State the preparation type.
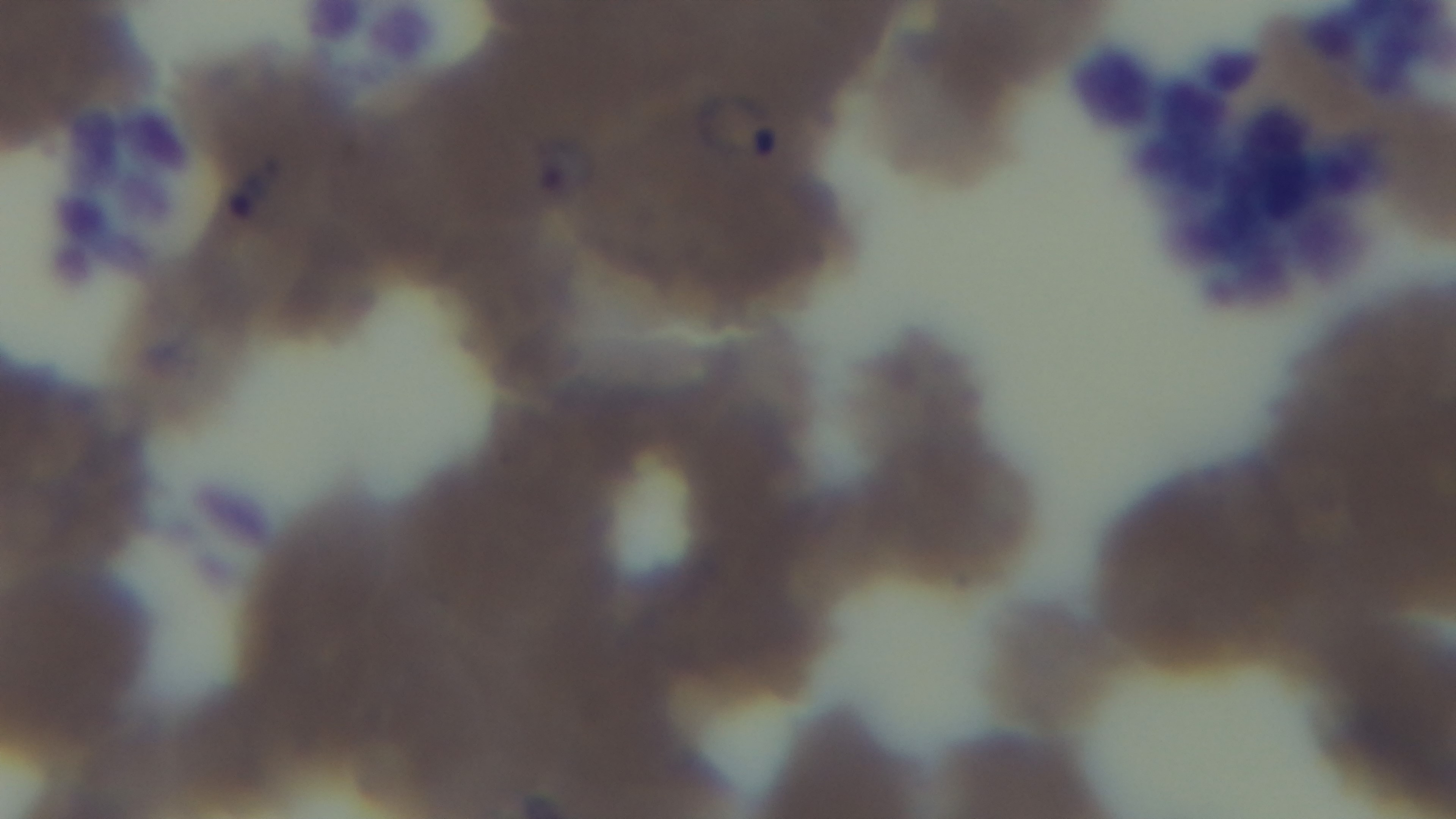

A thin smear.

One field from the slide. Giemsa stain. Malaria status: infected. Light microscopy. Captured with a mounted 4K digital camera. 100x oil-immersion objective.